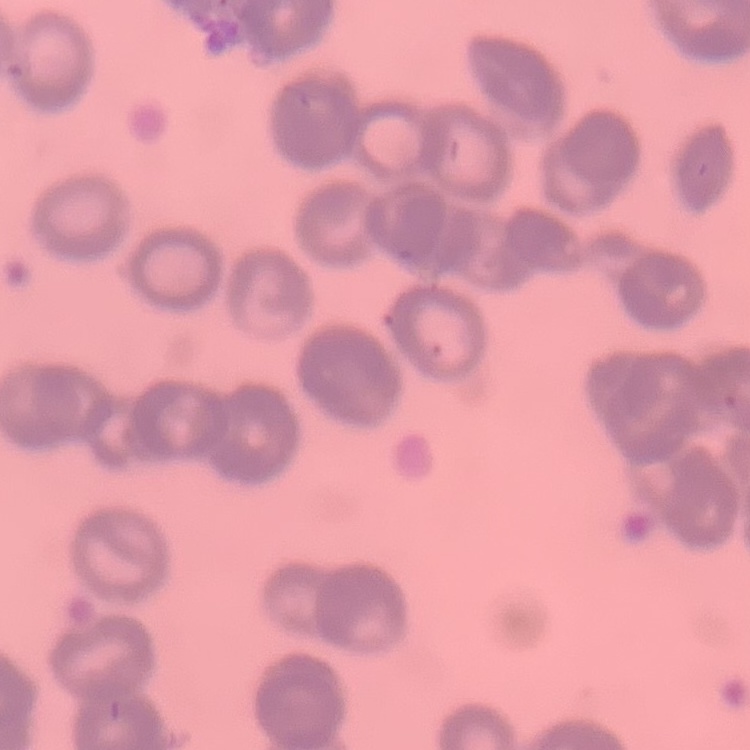

erythrocyte morphology = rouleaux formation
stain = Field's or Giemsa
image type = square crop of a larger photomicrograph
preparation = thin peripheral smear